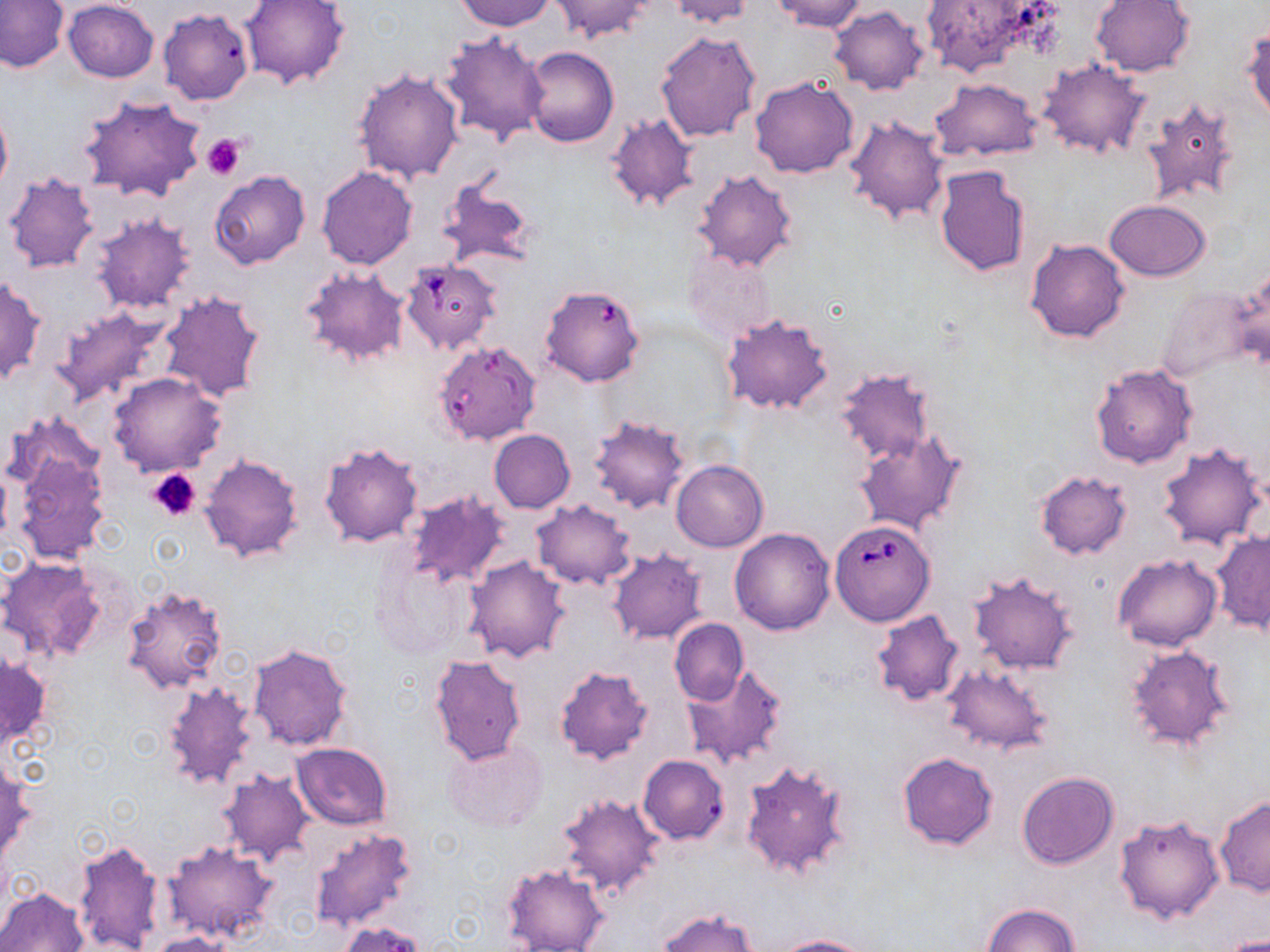
slide-level diagnosis = Babesia divergens
preparation = thin blood smear
magnification = 1000x
Babesia divergens-infected red blood cell locations = approximate bounding boxes as (x1, y1, x2, y2) in pixels: (400, 258, 501, 356), (540, 283, 647, 388), (431, 339, 541, 445), (831, 520, 935, 626)
uninfected red blood cell locations = approximate bounding boxes as (x1, y1, x2, y2) in pixels: (0, 0, 70, 72), (240, 0, 349, 89), (456, 0, 555, 31), (550, 0, 654, 43), (662, 0, 757, 27), (769, 0, 869, 32), (1090, 0, 1195, 76), (62, 1, 158, 82), (919, 1, 1053, 79), (829, 6, 930, 96), (158, 9, 254, 105), (1243, 25, 1270, 123), (438, 30, 551, 144), (655, 31, 760, 144), (522, 46, 619, 148), (1037, 58, 1151, 159), (352, 68, 464, 184), (749, 76, 859, 178), (931, 79, 1043, 161), (78, 94, 206, 203), (1140, 95, 1242, 208), (0, 98, 12, 199), (605, 112, 699, 211), (844, 114, 949, 225), (934, 165, 1030, 278), (209, 170, 311, 268), (693, 170, 799, 271), (3, 171, 99, 273), (433, 176, 539, 272), (1105, 199, 1211, 281), (91, 212, 196, 314), (1026, 238, 1130, 343), (680, 247, 776, 344), (1230, 266, 1270, 375), (300, 268, 412, 369), (0, 275, 46, 385), (1155, 281, 1259, 385), (158, 290, 267, 404), (51, 303, 170, 408), (721, 312, 834, 416), (1090, 363, 1197, 468), (833, 368, 935, 468), (109, 371, 226, 476), (588, 415, 691, 513), (488, 429, 575, 513), (854, 431, 967, 536), (10, 435, 110, 565), (320, 441, 425, 549), (1157, 441, 1267, 550), (199, 453, 304, 562), (671, 459, 768, 551), (1035, 470, 1132, 559), (404, 491, 513, 589), (530, 499, 636, 590), (729, 528, 835, 634), (1211, 530, 1269, 633), (607, 548, 708, 644), (1112, 553, 1221, 651), (372, 554, 475, 658), (462, 556, 571, 662), (0, 557, 109, 664), (966, 570, 1078, 674), (121, 583, 227, 693), (870, 609, 964, 706), (669, 619, 748, 705), (1124, 643, 1237, 753), (248, 644, 353, 750), (0, 650, 48, 750), (428, 653, 528, 765), (941, 664, 1052, 755), (554, 666, 653, 764), (682, 666, 787, 770), (163, 681, 261, 791), (444, 738, 548, 833), (292, 743, 392, 830), (897, 751, 998, 851), (1, 753, 33, 865), (637, 754, 730, 844), (738, 759, 854, 882), (216, 769, 313, 865), (1017, 772, 1119, 869), (556, 792, 666, 900), (1215, 796, 1270, 897), (1113, 811, 1225, 925), (307, 826, 419, 932), (73, 838, 165, 952), (163, 842, 278, 944), (500, 862, 609, 951), (1, 887, 89, 952), (982, 904, 1079, 952), (657, 907, 757, 952), (339, 921, 427, 952), (149, 931, 236, 952), (771, 934, 873, 952), (1213, 935, 1269, 952)
field of view = single
platelet locations = approximate bounding boxes as (x1, y1, x2, y2) in pixels: (202, 132, 247, 179), (148, 467, 202, 522)
modality = light microscopy
stain = May-Grünwald-Giemsa
image size = 1270×952 pixels